Assess this cell for malaria.
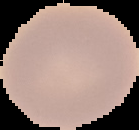
It is uninfected.

image_type: segmented cell region with the area outside set to black
image_size: 139×130 pixels
preparation: thin blood film